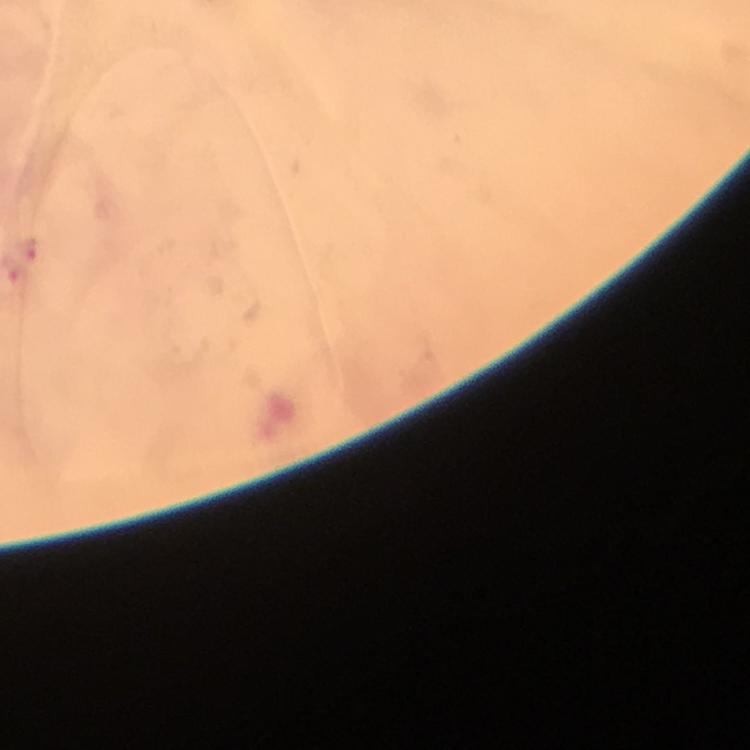

malaria parasite locations = approximate centers as {x, y} in pixels: {31, 248}, {13, 270}
cropped from = a single field of view
preparation = thick smear
immersion oil = applied
stain = Giemsa
image size = 750×750 pixels
capture = smartphone photograph through a microscope
context = from a malaria diagnostic workup
magnification = 100x